Classify this cell by malaria status.
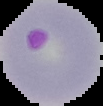

Parasitized.

From a thin blood smear. The area outside the segmented cell region is set to black. Image is 103×106 pixels.